Outline each Babesia divergens-infected red blood cell.
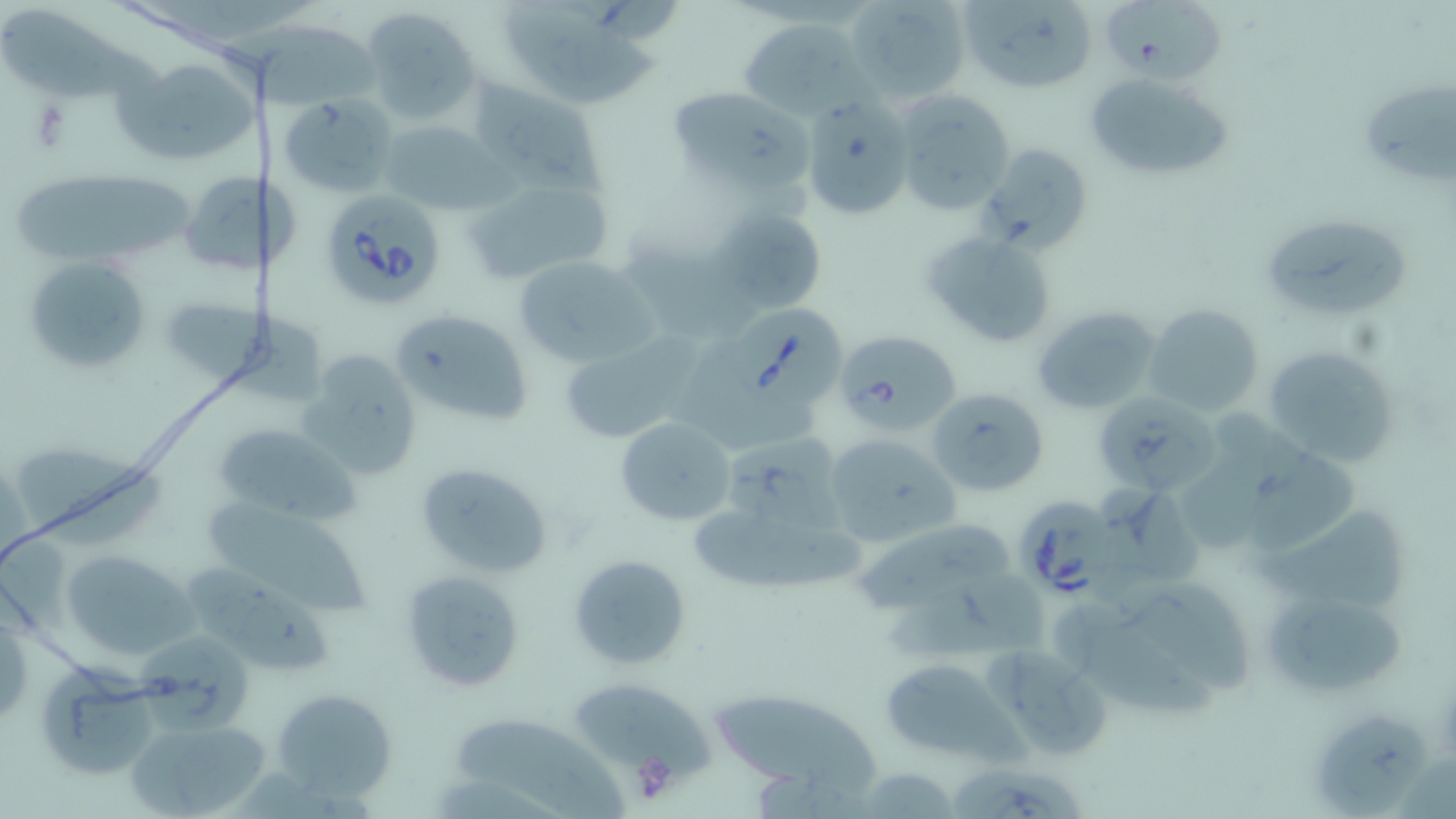

Approximate bounding boxes as [x1, y1, x2, y2] in pixels.
Babesia divergens-infected red blood cells: [318, 187, 446, 309], [723, 303, 847, 412], [834, 329, 959, 435], [1015, 497, 1114, 602].

Uninfected red blood cell locations: [844, 0, 971, 105], [958, 0, 1099, 94], [1099, 2, 1234, 90], [501, 3, 670, 111], [363, 7, 481, 126], [0, 10, 165, 101], [738, 16, 867, 117], [210, 19, 388, 114], [110, 56, 255, 169], [1083, 71, 1229, 181], [1358, 78, 1456, 186], [474, 83, 598, 193], [664, 84, 812, 194], [893, 91, 1017, 215], [282, 97, 395, 195], [803, 102, 913, 221], [376, 117, 501, 216], [978, 141, 1095, 256], [178, 172, 306, 277], [464, 172, 615, 289], [14, 173, 197, 268], [712, 209, 827, 315], [1260, 213, 1415, 325], [921, 228, 1057, 349], [619, 239, 760, 342], [25, 253, 153, 374], [512, 254, 654, 366], [160, 295, 329, 401], [1144, 303, 1265, 418], [1031, 305, 1165, 415], [391, 308, 533, 426], [559, 337, 692, 446], [1265, 343, 1400, 469], [293, 350, 423, 482], [683, 353, 816, 454], [926, 386, 1049, 496], [1092, 388, 1220, 496], [1180, 402, 1301, 554], [616, 416, 737, 526], [212, 421, 361, 527], [822, 432, 959, 550], [719, 433, 850, 540], [14, 442, 169, 553], [412, 461, 555, 579], [1102, 484, 1200, 589], [199, 498, 376, 616], [687, 501, 870, 597], [1258, 508, 1404, 610], [849, 517, 1019, 612], [60, 548, 199, 662], [568, 554, 693, 671], [182, 559, 331, 673], [1099, 560, 1253, 699], [399, 568, 528, 695], [1261, 585, 1406, 699], [1052, 588, 1223, 716], [0, 607, 32, 729], [142, 632, 253, 739], [978, 643, 1116, 759], [878, 655, 1016, 762], [43, 661, 157, 778], [567, 682, 715, 779], [271, 688, 402, 806], [713, 693, 883, 798], [1315, 706, 1433, 807], [457, 716, 627, 818], [131, 718, 269, 815], [950, 763, 1092, 818], [851, 767, 961, 817]. Platelet locations: [27, 101, 75, 151], [630, 751, 680, 804]. Slide-level diagnosis: Babesia divergens. Image is 1456×819 pixels. May-Grünwald-Giemsa stain. Thin blood film. Captured at 1000x magnification. Optical microscopy. One field of a larger specimen.